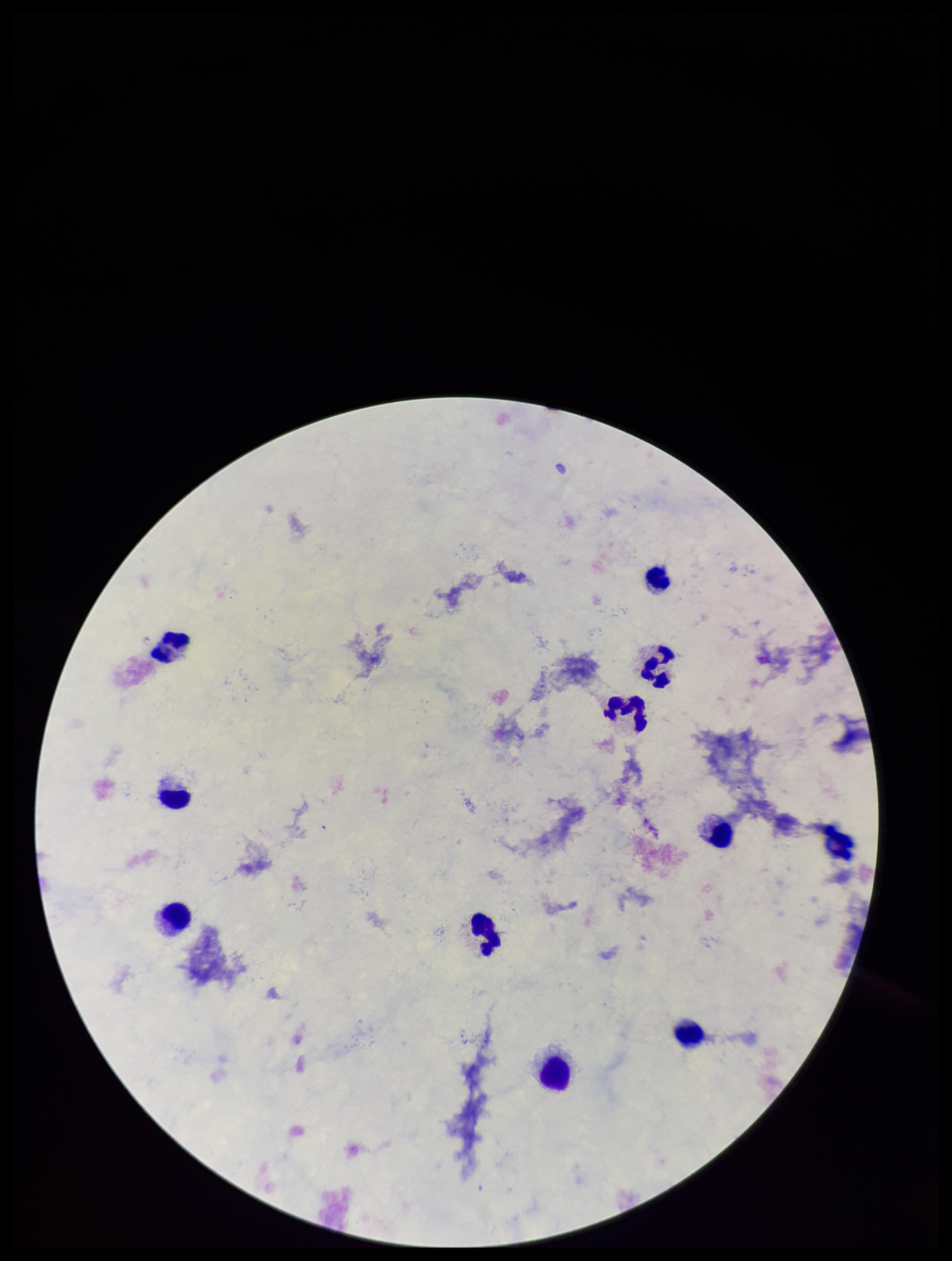 Parasite count: 0. Leukocyte count: 10. Plasmodium parasites: none detected. Patient malaria status: negative. Preparation: thick blood smear. Stained with Giemsa. Image is 952×1261 pixels. Photographed through the microscope eyepiece with a smartphone camera. Single field of view.